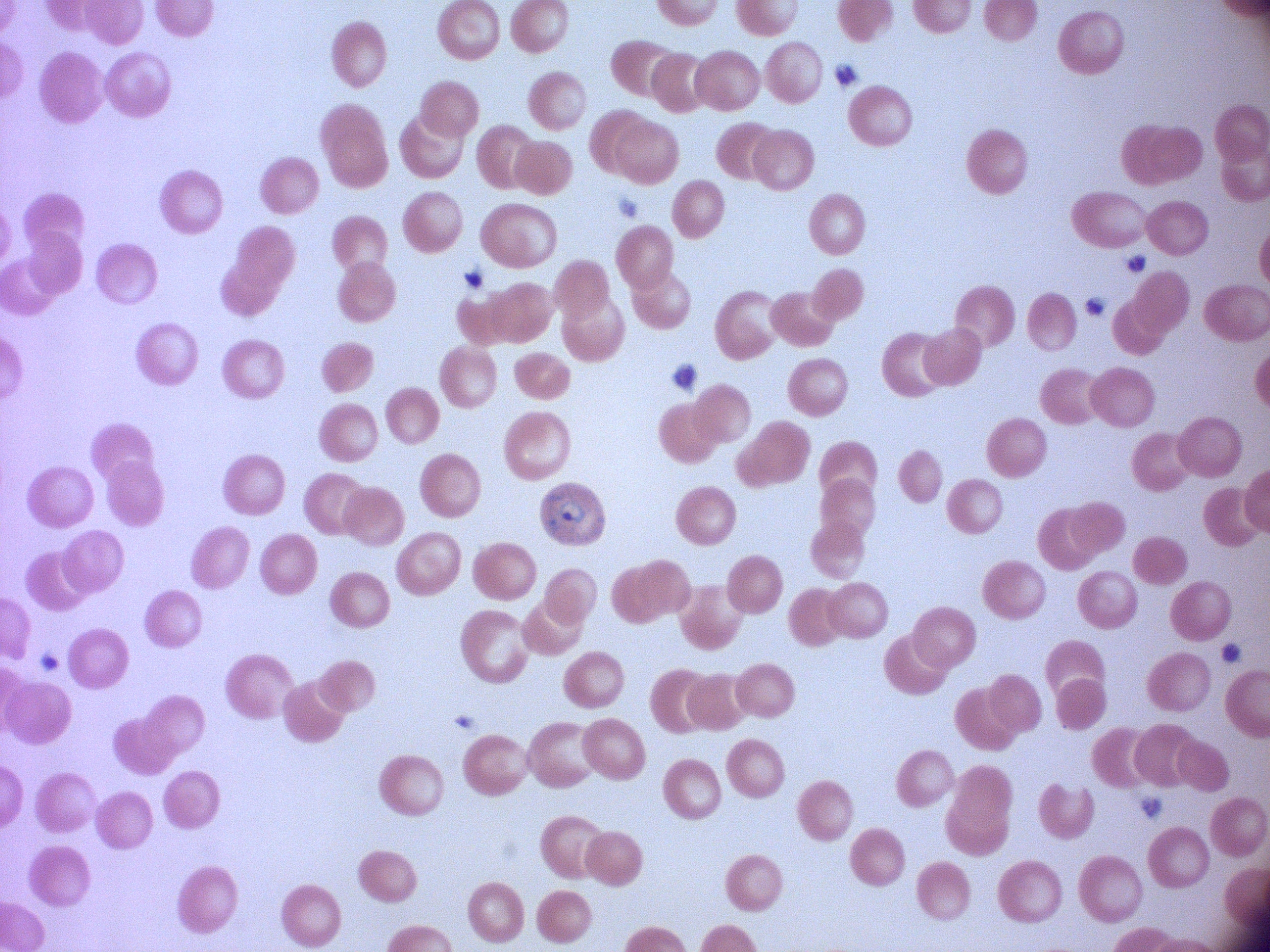

Approximate bounding boxes as (x1, y1, x2, y2) in pixels, from the source annotation, which is not necessarily exhaustive. Ring form locations: (533, 475, 613, 550). Captured at 100x magnification. Giemsa stain. Thin blood smear. Species: Plasmodium falciparum. Image is 1270×952 pixels. Single field of view. Acquired with a Leica DM2000 optical microscope and its built-in camera.